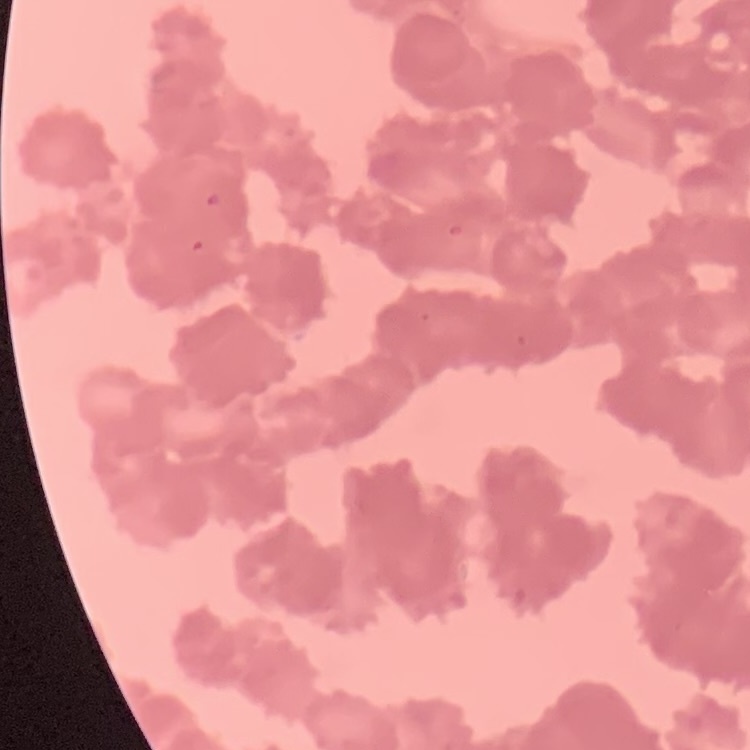
Summary:
  - Erythrocyte morphology: rouleaux formation
  - Preparation: thin blood film
  - Image type: one tile cut from a larger photomicrograph
  - Stain: Field's or Giemsa